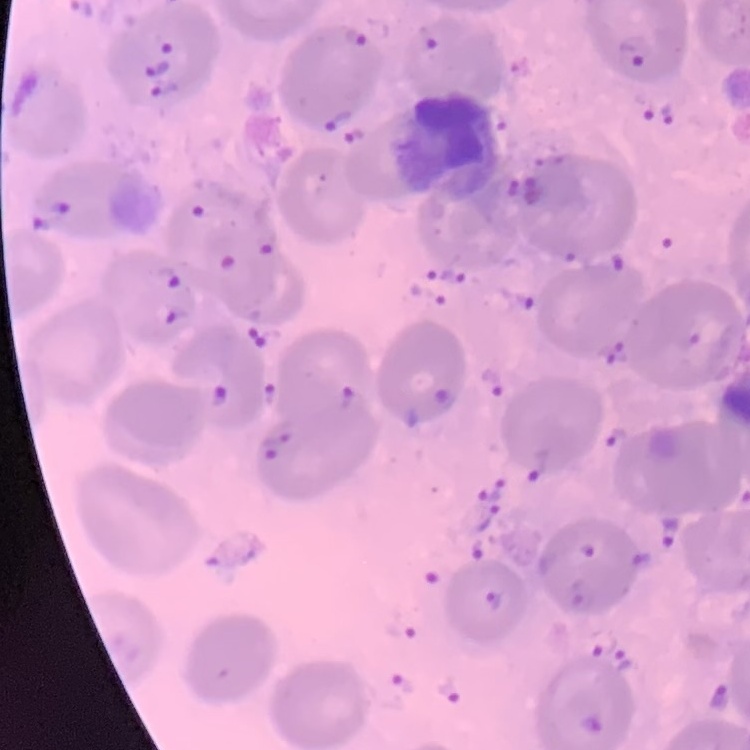
red blood cell morphology = no rouleaux formation
image type = square crop of a larger photomicrograph
stain = Field's or Giemsa
preparation = thin blood film